Classify this cell by malaria status.
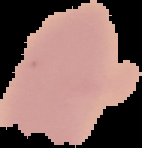

Uninfected.

{
  "image_size": "142×148 pixels",
  "preparation": "thin blood smear",
  "image_type": "cell region segmented out of the field of view; surrounding area masked to black"
}